Locate every Plasmodium parasite.
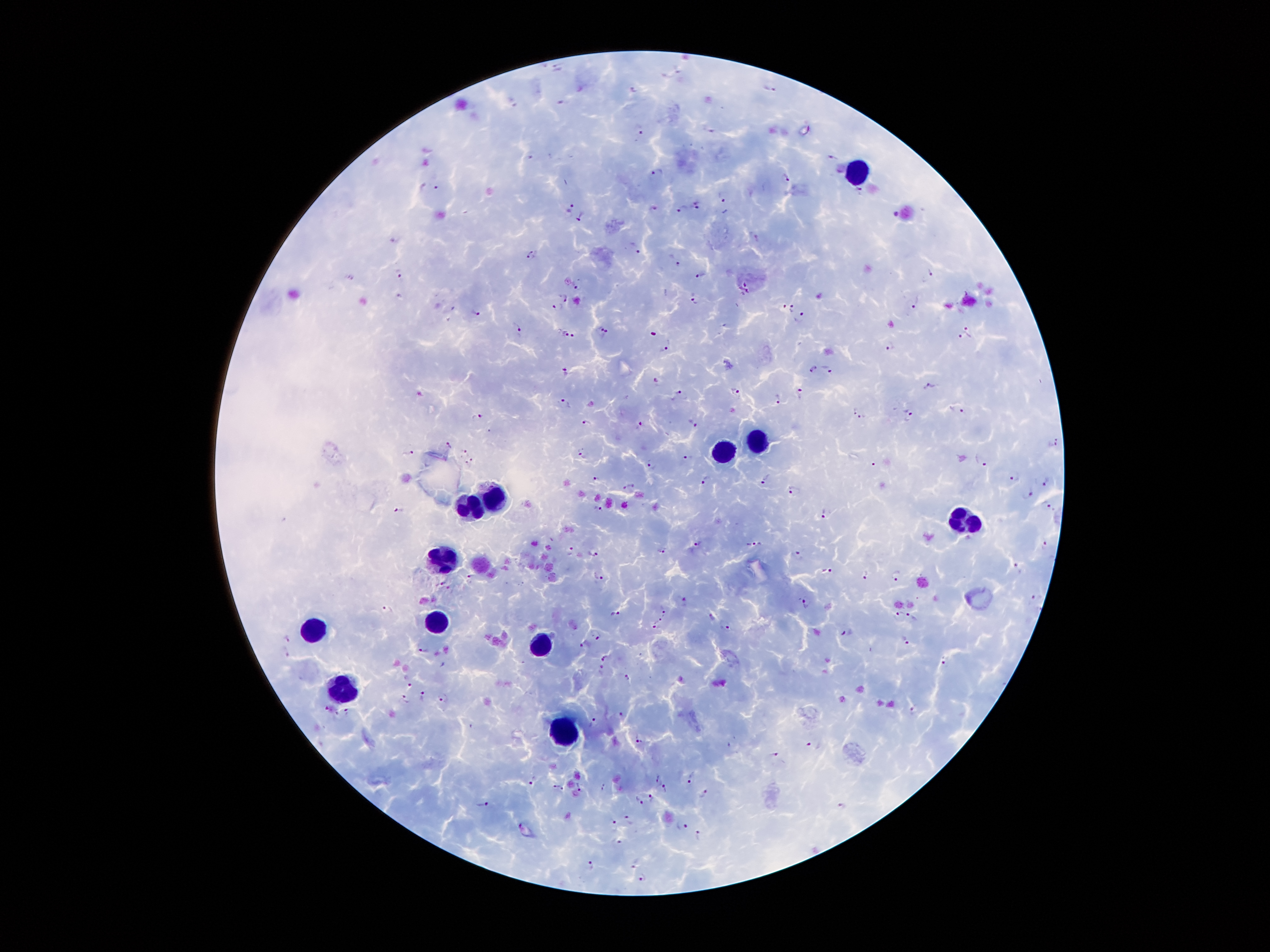

Approximate centers as (x, y) in pixels.
Plasmodium parasites: (558, 66), (678, 69), (771, 89), (635, 91), (563, 102), (514, 104), (639, 130), (833, 155), (530, 157), (657, 172), (787, 177), (436, 187), (861, 189), (722, 196), (697, 204), (572, 208), (654, 208), (683, 208), (580, 216), (751, 234), (532, 249), (639, 252), (531, 258), (679, 264), (397, 272), (931, 272), (701, 275), (577, 288), (565, 297), (694, 300), (915, 303), (559, 306), (785, 306), (792, 308), (477, 313), (803, 317), (598, 326), (518, 327), (967, 327), (566, 334), (607, 334), (573, 335), (965, 337), (668, 345), (889, 345), (813, 368), (827, 369), (566, 372), (656, 381), (929, 386), (736, 391), (798, 393), (682, 394), (776, 396), (565, 402), (957, 410), (855, 411), (909, 412), (477, 417), (863, 417), (692, 421), (639, 422), (587, 424), (1054, 441), (449, 444), (464, 449), (409, 452), (584, 452), (686, 457), (468, 462), (981, 462), (651, 463), (874, 463), (1014, 477), (764, 479), (597, 480), (706, 480), (1046, 482), (629, 486), (793, 490), (1029, 493), (1047, 503), (597, 507), (399, 511), (823, 514), (698, 542), (1046, 543), (754, 544), (570, 549), (660, 549), (594, 553), (798, 554), (1017, 565), (826, 570), (599, 575), (865, 575), (896, 576), (470, 578), (1033, 597), (684, 600), (806, 602), (388, 606), (663, 612), (613, 613), (896, 613), (913, 614), (711, 616), (660, 617), (726, 623), (655, 624), (848, 630), (596, 633), (288, 639), (907, 639), (586, 645), (424, 651), (286, 652), (606, 657), (944, 658), (600, 668), (626, 675), (408, 680), (422, 693), (407, 698), (442, 698), (328, 709), (914, 711), (347, 712), (622, 714), (595, 721), (638, 738), (815, 742), (774, 750), (657, 777), (692, 778), (533, 782), (559, 786), (604, 786), (665, 787), (703, 793), (651, 797), (640, 798), (482, 803), (842, 805), (629, 819), (683, 822), (614, 826), (699, 836), (620, 840), (634, 863), (589, 865), (643, 878).

leukocyte locations = (856, 171), (754, 442), (721, 450), (499, 495), (466, 511), (960, 524), (444, 562), (437, 615), (319, 622), (539, 639), (343, 695), (563, 730)
field of view = single
magnification = 100x
capture = smartphone camera through the microscope eyepiece
patient malaria status = infected with Plasmodium falciparum
stain = Giemsa
preparation = thick blood film
image size = 1270×952 pixels